Classify this cell by malaria status.
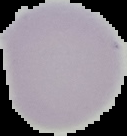
It is uninfected.

Summary:
  - Image type: segmented cell region with the area outside set to black
  - Preparation: thin blood smear
  - Image size: 127×136 pixels